Give the position of every Plasmodium parasite.
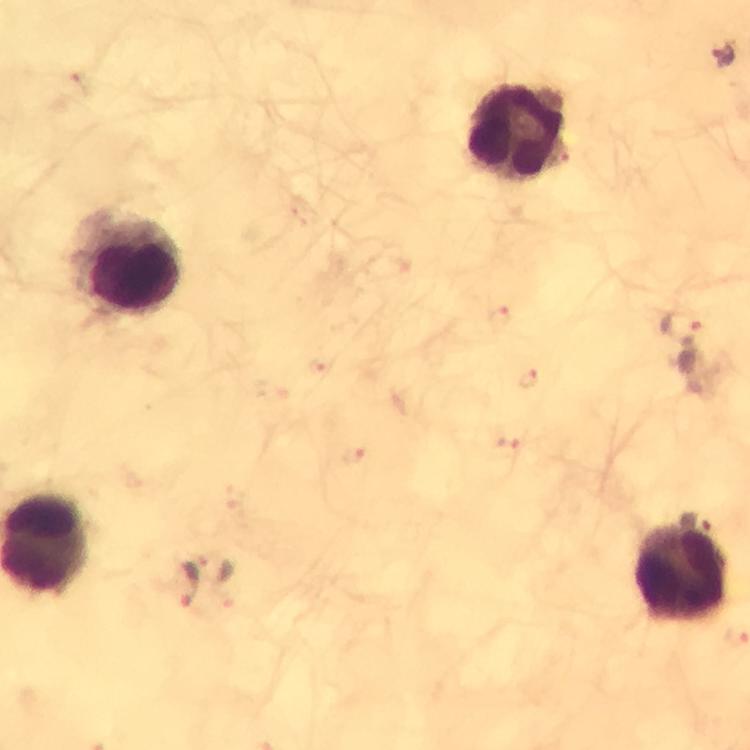
Approximate centers as (x, y) in pixels.
Plasmodium parasites: (722, 55), (499, 315), (681, 328), (528, 379), (354, 455), (214, 568), (187, 584).

Summary:
  - Leukocyte locations: (519, 129), (129, 264), (681, 575)
  - Context: from a diagnostic examination for malaria
  - Capture: smartphone mounted on the microscope
  - Image size: 750×750 pixels
  - Cropped from: a single field of view
  - Preparation: thick blood film
  - Stain: Giemsa
  - Magnification: 100x
  - Immersion oil: applied